Report the malaria status of this cell.
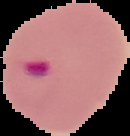
It is parasitized.

preparation = thin blood smear
image size = 130×136 pixels
image type = segmented cell region on a black background